Outline each blood parasite and name the species.
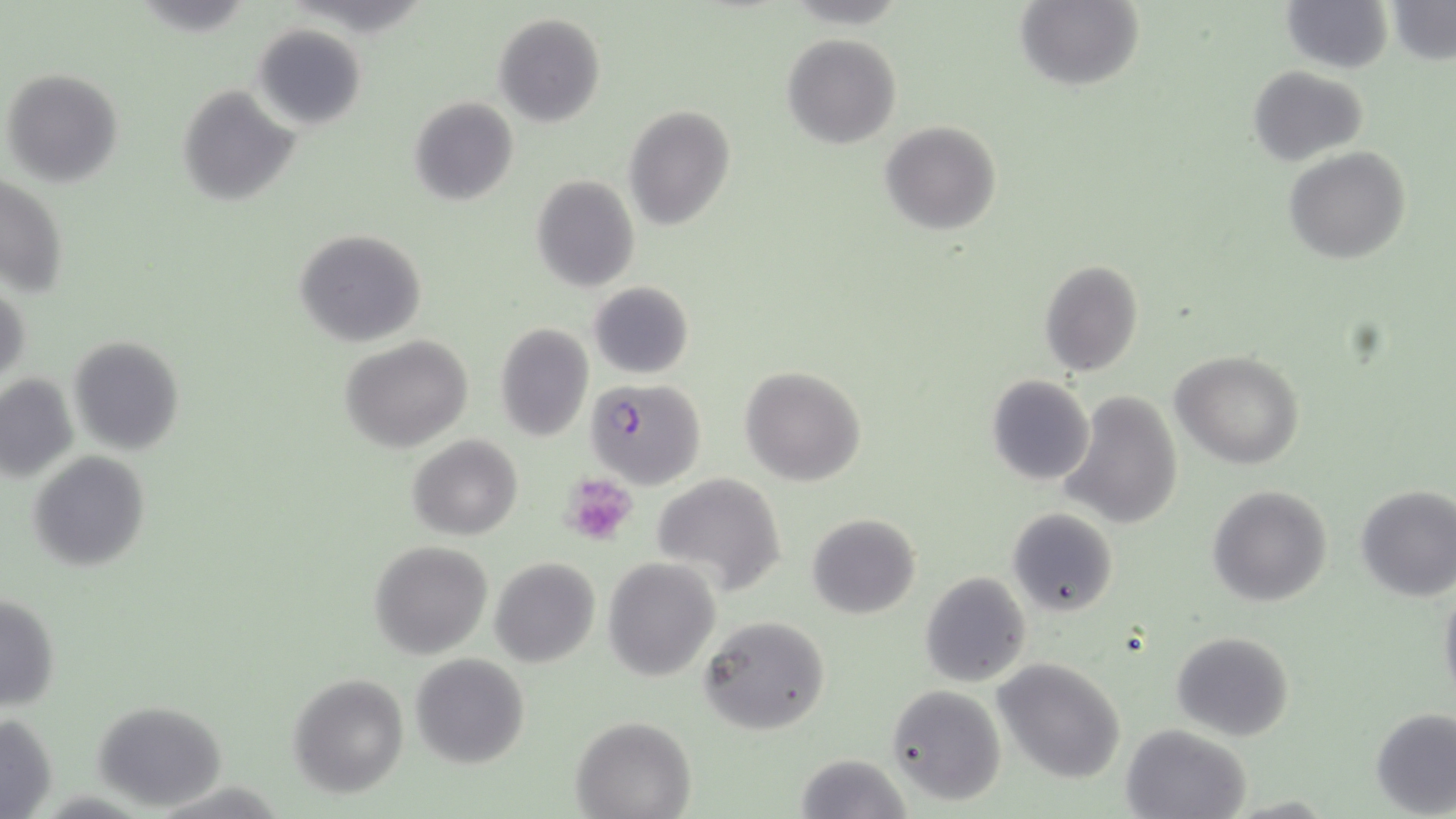

Approximate bounding boxes as named x1/y1/x2/y2 corners in pixels.
Plasmodium falciparum-infected red blood cells: (x1=584, y1=378, x2=705, y2=489).
No Plasmodium ovale, Plasmodium malariae, Plasmodium vivax, Babesia divergens, or Trypanosoma brucei observed.

Uninfected red blood cell locations: (x1=1016, y1=0, x2=1144, y2=92), (x1=1282, y1=0, x2=1392, y2=73), (x1=1388, y1=1, x2=1455, y2=65), (x1=494, y1=13, x2=605, y2=128), (x1=253, y1=23, x2=367, y2=130), (x1=782, y1=33, x2=901, y2=150), (x1=1248, y1=65, x2=1368, y2=166), (x1=2, y1=67, x2=124, y2=186), (x1=176, y1=83, x2=301, y2=205), (x1=408, y1=96, x2=519, y2=207), (x1=623, y1=105, x2=734, y2=230), (x1=879, y1=120, x2=1001, y2=236), (x1=1285, y1=147, x2=1410, y2=264), (x1=0, y1=174, x2=69, y2=301), (x1=532, y1=174, x2=640, y2=293), (x1=292, y1=229, x2=427, y2=347), (x1=1038, y1=259, x2=1144, y2=377), (x1=1, y1=279, x2=31, y2=387), (x1=588, y1=281, x2=694, y2=379), (x1=494, y1=322, x2=594, y2=441), (x1=68, y1=335, x2=185, y2=456), (x1=341, y1=336, x2=473, y2=454), (x1=1172, y1=350, x2=1305, y2=468), (x1=740, y1=365, x2=867, y2=485), (x1=0, y1=372, x2=79, y2=483), (x1=987, y1=375, x2=1094, y2=487), (x1=1061, y1=391, x2=1185, y2=530), (x1=409, y1=434, x2=524, y2=540), (x1=28, y1=451, x2=150, y2=571), (x1=650, y1=472, x2=787, y2=596), (x1=1355, y1=483, x2=1456, y2=601), (x1=1205, y1=485, x2=1334, y2=607), (x1=1008, y1=507, x2=1118, y2=617), (x1=806, y1=512, x2=921, y2=618), (x1=369, y1=541, x2=492, y2=658), (x1=489, y1=557, x2=600, y2=668), (x1=603, y1=557, x2=720, y2=679), (x1=919, y1=571, x2=1032, y2=689), (x1=1439, y1=581, x2=1456, y2=710), (x1=0, y1=593, x2=61, y2=709), (x1=700, y1=615, x2=831, y2=736), (x1=1172, y1=631, x2=1295, y2=741), (x1=410, y1=653, x2=529, y2=769), (x1=995, y1=659, x2=1125, y2=785), (x1=288, y1=674, x2=409, y2=798), (x1=886, y1=683, x2=1007, y2=807), (x1=92, y1=699, x2=227, y2=810), (x1=1371, y1=706, x2=1456, y2=816), (x1=0, y1=712, x2=58, y2=819), (x1=572, y1=715, x2=694, y2=819), (x1=1121, y1=724, x2=1249, y2=819), (x1=795, y1=752, x2=912, y2=819). Platelet locations: (x1=562, y1=473, x2=637, y2=543). Slide-level diagnosis: Plasmodium falciparum. Single field of view. Captured at 1000x magnification. Light microscopy. Image is 1456×819 pixels. May-Grünwald-Giemsa-stained preparation. Thin blood smear.